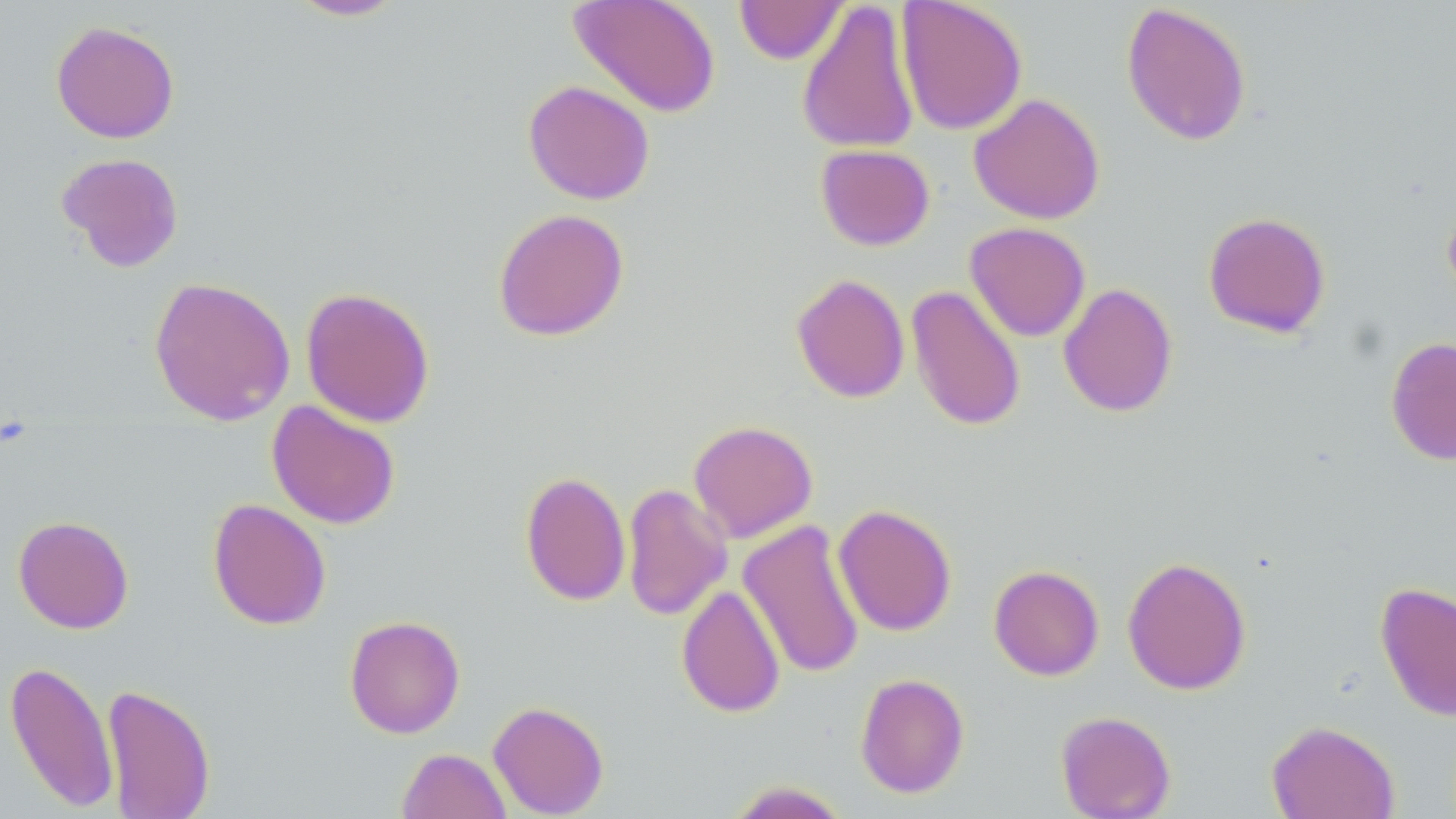
slide_level_diagnosis: no evidence of blood parasites
image_size: 1456×819 pixels
uninfected_red_blood_cell_locations: 'approximate bounding boxes as [x1, y1, x2, y2] in pixels: [284, 0, 409, 22], [568, 0, 721, 118], [797, 0, 921, 155], [896, 0, 1027, 136], [734, 1, 848, 64], [1120, 2, 1252, 147], [51, 20, 180, 144], [522, 80, 655, 205], [968, 93, 1105, 225], [815, 144, 935, 251], [55, 152, 184, 272], [492, 207, 630, 342], [1202, 211, 1331, 338], [964, 222, 1090, 341], [790, 273, 910, 403], [148, 276, 296, 426], [1058, 283, 1178, 418], [906, 284, 1027, 432], [300, 287, 436, 428], [1385, 336, 1456, 466], [266, 400, 401, 529], [688, 419, 818, 543], [519, 471, 631, 606], [621, 483, 733, 622], [207, 498, 331, 631], [833, 503, 957, 637], [13, 515, 134, 634], [738, 519, 865, 679], [1122, 556, 1251, 695], [989, 564, 1104, 681], [1375, 582, 1456, 721], [676, 584, 785, 718], [344, 614, 466, 738], [4, 660, 120, 812], [855, 673, 970, 798], [101, 683, 216, 819], [488, 700, 609, 817], [1055, 710, 1176, 819], [1266, 719, 1400, 819], [397, 747, 511, 819], [723, 780, 852, 819]'
modality: light microscopy
preparation: thin blood smear
stain: May-Grünwald-Giemsa
field_of_view: single
magnification: 1000x